Name the parasite shown.
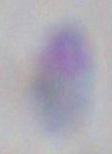

Toxoplasma gondii.

Summary:
  - Modality: micrograph
  - Magnification: 1000x